Assess the morphology of the red blood cells.
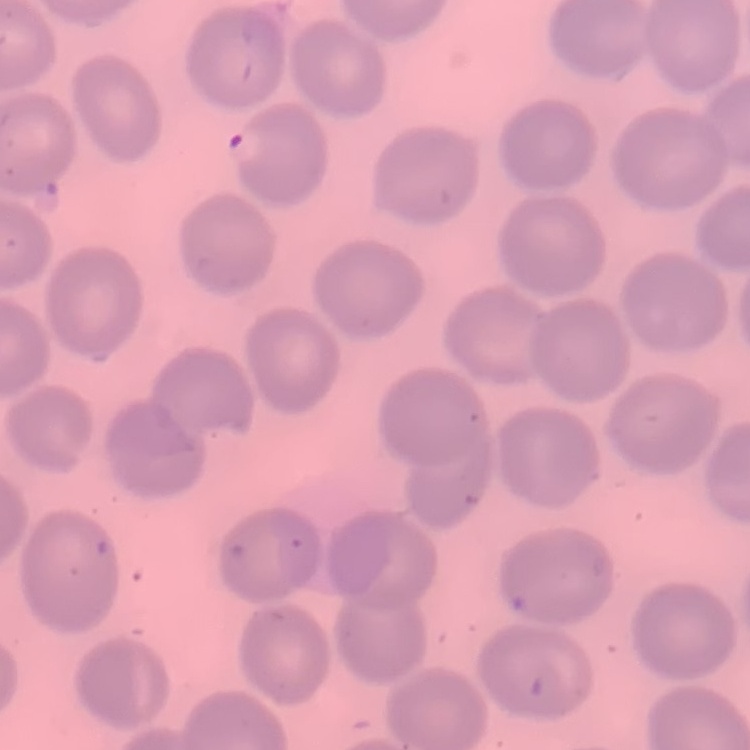

No rouleaux formation.

Stained with either Field's or Giemsa. Thin blood smear. One tile cut from a larger photomicrograph.